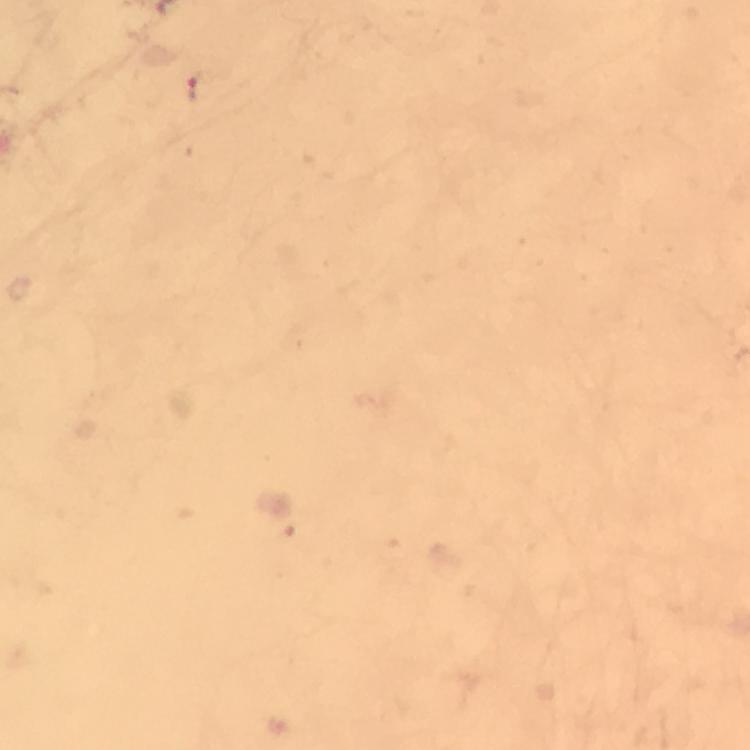

Approximate centers as [x, y] in pixels. Plasmodium parasite locations: [200, 86]. From a malaria diagnostic workup. Giemsa-stained preparation. Immersion oil was used. Cropped region of a single field of view. Thick smear. 100x magnification. Image is 750×750 pixels. Photographed through the microscope with a smartphone camera.